Locate every uninfected red blood cell.
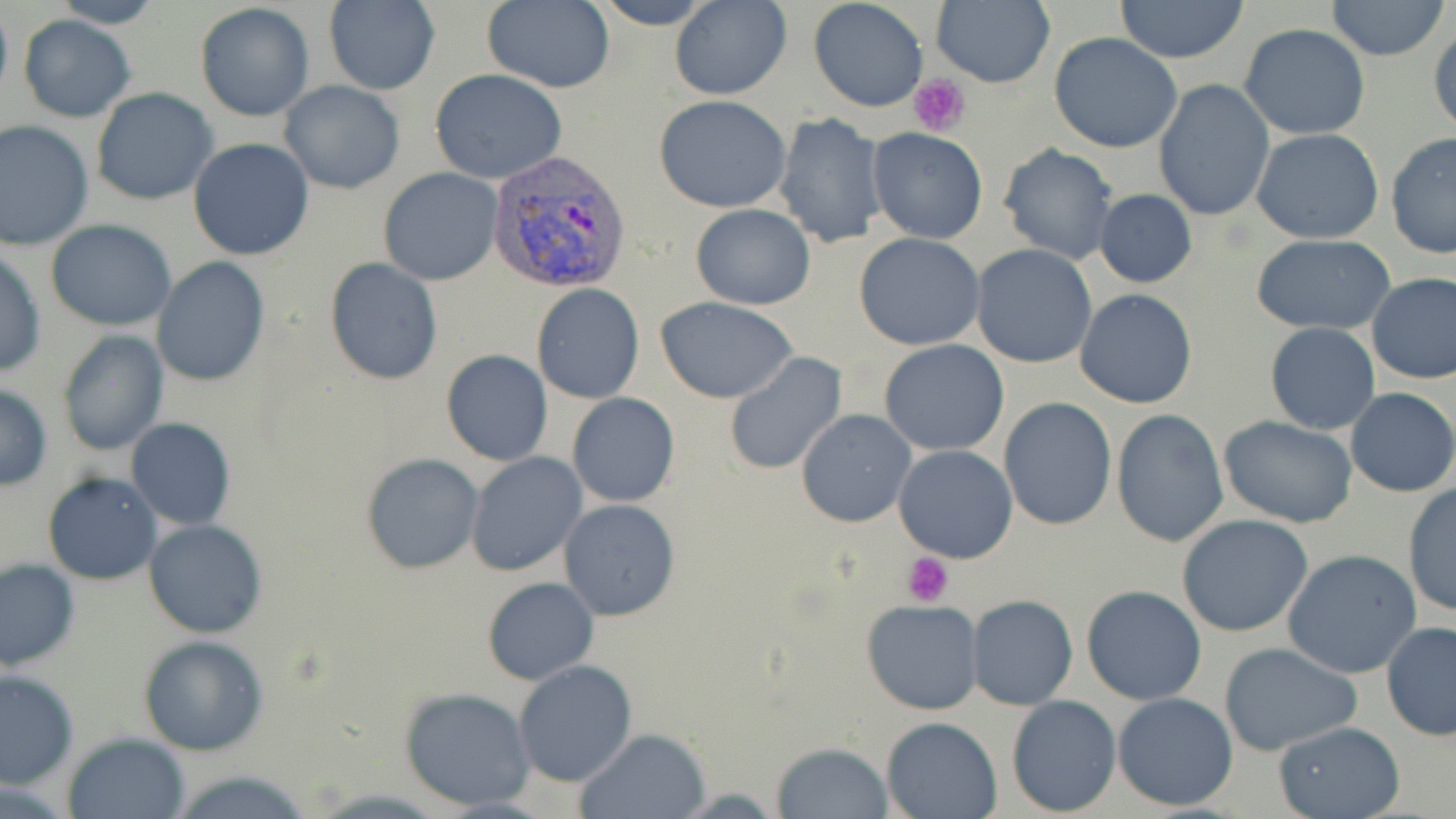

Approximate bounding boxes as named x1/y1/x2/y2 corners in pixels.
Uninfected red blood cells: (x1=46, y1=0, x2=166, y2=28), (x1=482, y1=0, x2=615, y2=93), (x1=590, y1=0, x2=717, y2=29), (x1=670, y1=0, x2=791, y2=99), (x1=808, y1=0, x2=929, y2=112), (x1=932, y1=0, x2=1055, y2=90), (x1=1115, y1=0, x2=1249, y2=63), (x1=0, y1=1, x2=13, y2=104), (x1=1325, y1=1, x2=1448, y2=61), (x1=194, y1=2, x2=315, y2=122), (x1=320, y1=2, x2=441, y2=94), (x1=18, y1=15, x2=135, y2=122), (x1=1428, y1=22, x2=1456, y2=137), (x1=1239, y1=23, x2=1370, y2=140), (x1=1049, y1=34, x2=1184, y2=153), (x1=429, y1=69, x2=566, y2=185), (x1=1152, y1=78, x2=1275, y2=222), (x1=281, y1=82, x2=404, y2=194), (x1=90, y1=88, x2=218, y2=206), (x1=653, y1=94, x2=792, y2=212), (x1=773, y1=111, x2=888, y2=249), (x1=0, y1=119, x2=95, y2=249), (x1=867, y1=128, x2=991, y2=244), (x1=1251, y1=128, x2=1385, y2=243), (x1=1386, y1=133, x2=1456, y2=260), (x1=188, y1=137, x2=315, y2=261), (x1=998, y1=144, x2=1119, y2=265), (x1=378, y1=167, x2=503, y2=286), (x1=1094, y1=189, x2=1198, y2=287), (x1=690, y1=203, x2=816, y2=310), (x1=45, y1=220, x2=178, y2=331), (x1=853, y1=232, x2=986, y2=350), (x1=1250, y1=235, x2=1396, y2=334), (x1=971, y1=244, x2=1095, y2=368), (x1=0, y1=249, x2=46, y2=379), (x1=153, y1=257, x2=270, y2=387), (x1=324, y1=258, x2=443, y2=386), (x1=1366, y1=272, x2=1456, y2=384), (x1=532, y1=283, x2=644, y2=403), (x1=1074, y1=290, x2=1199, y2=409), (x1=656, y1=296, x2=800, y2=404), (x1=1264, y1=322, x2=1380, y2=434), (x1=57, y1=330, x2=168, y2=456), (x1=879, y1=338, x2=1009, y2=455), (x1=442, y1=350, x2=552, y2=465), (x1=724, y1=352, x2=848, y2=475), (x1=0, y1=382, x2=52, y2=490), (x1=1345, y1=388, x2=1456, y2=497), (x1=568, y1=392, x2=680, y2=508), (x1=998, y1=397, x2=1117, y2=531), (x1=797, y1=409, x2=917, y2=527), (x1=1112, y1=410, x2=1229, y2=548), (x1=1220, y1=417, x2=1359, y2=529), (x1=126, y1=419, x2=236, y2=531), (x1=893, y1=445, x2=1018, y2=563), (x1=466, y1=453, x2=587, y2=577), (x1=360, y1=454, x2=485, y2=574), (x1=43, y1=472, x2=161, y2=585), (x1=1402, y1=482, x2=1456, y2=616), (x1=558, y1=498, x2=682, y2=621), (x1=1176, y1=515, x2=1315, y2=639), (x1=144, y1=519, x2=267, y2=637), (x1=1283, y1=549, x2=1423, y2=679), (x1=0, y1=558, x2=80, y2=669), (x1=481, y1=575, x2=600, y2=686), (x1=1082, y1=585, x2=1206, y2=706), (x1=968, y1=594, x2=1078, y2=710), (x1=862, y1=599, x2=982, y2=714), (x1=1381, y1=620, x2=1456, y2=740), (x1=139, y1=635, x2=270, y2=755), (x1=1218, y1=642, x2=1362, y2=755), (x1=514, y1=660, x2=637, y2=786), (x1=0, y1=669, x2=78, y2=788), (x1=398, y1=686, x2=538, y2=811), (x1=1111, y1=693, x2=1239, y2=809), (x1=1007, y1=694, x2=1121, y2=815), (x1=879, y1=716, x2=1002, y2=819), (x1=1272, y1=720, x2=1405, y2=818), (x1=574, y1=728, x2=710, y2=818), (x1=65, y1=733, x2=189, y2=819), (x1=771, y1=742, x2=893, y2=818), (x1=167, y1=768, x2=313, y2=819).

slide-level diagnosis = Plasmodium vivax
platelet locations = approximate bounding boxes as named x1/y1/x2/y2 corners in pixels: (x1=908, y1=74, x2=970, y2=137), (x1=901, y1=552, x2=953, y2=606)
magnification = 1000x
modality = light microscopy
Plasmodium vivax-infected red blood cell locations = approximate bounding boxes as named x1/y1/x2/y2 corners in pixels: (x1=487, y1=151, x2=632, y2=291)
image size = 1456×819 pixels
preparation = thin blood smear
field of view = single
stain = May-Grünwald-Giemsa